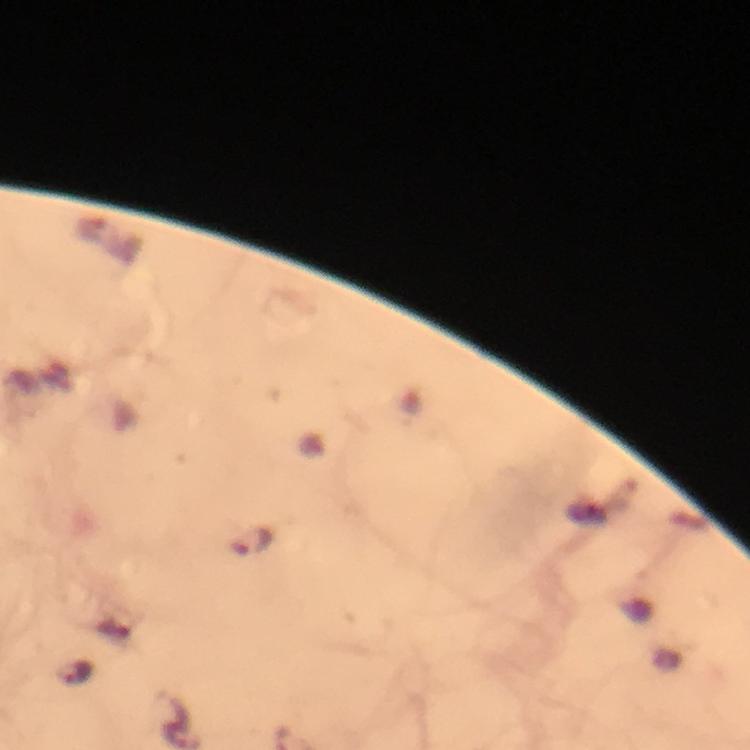 Approximate centers as {x, y} in pixels. Malaria parasite locations: {254, 542}. A crop from one field of view. Thick smear. Photographed through the microscope with a smartphone camera. Immersion oil was used. Image is 750×750 pixels. Giemsa-stained preparation. From a diagnostic examination for malaria. 100x magnification.